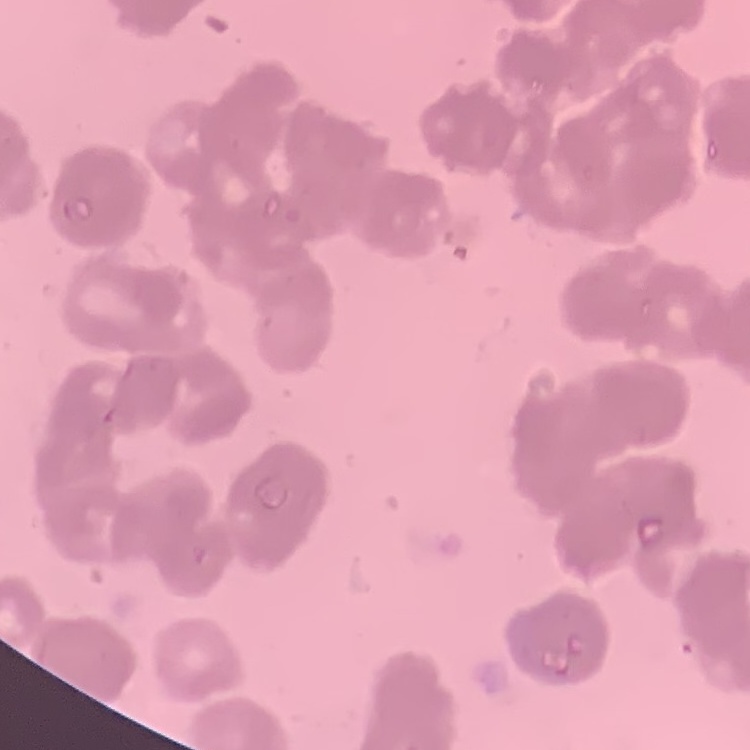

Summary:
  - Red blood cell morphology: rouleaux formation
  - Image type: square crop of a larger photomicrograph
  - Stain: Field's or Giemsa
  - Preparation: thin blood film